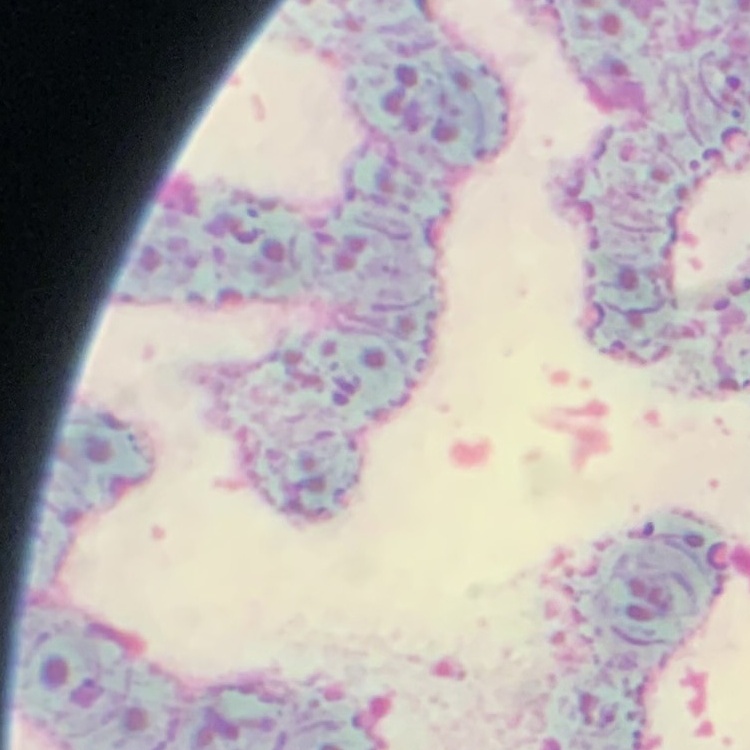
red_blood_cell_morphology: rouleaux formation
preparation: thin blood smear
stain: Field's or Giemsa
image_type: square crop of a larger photomicrograph